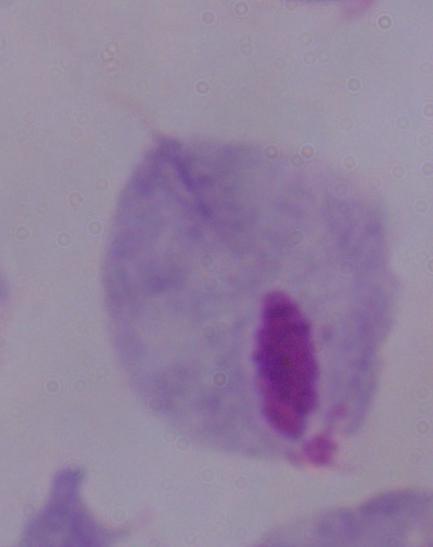 Micrograph. Captured at 1000x magnification. A trichomonad is shown.